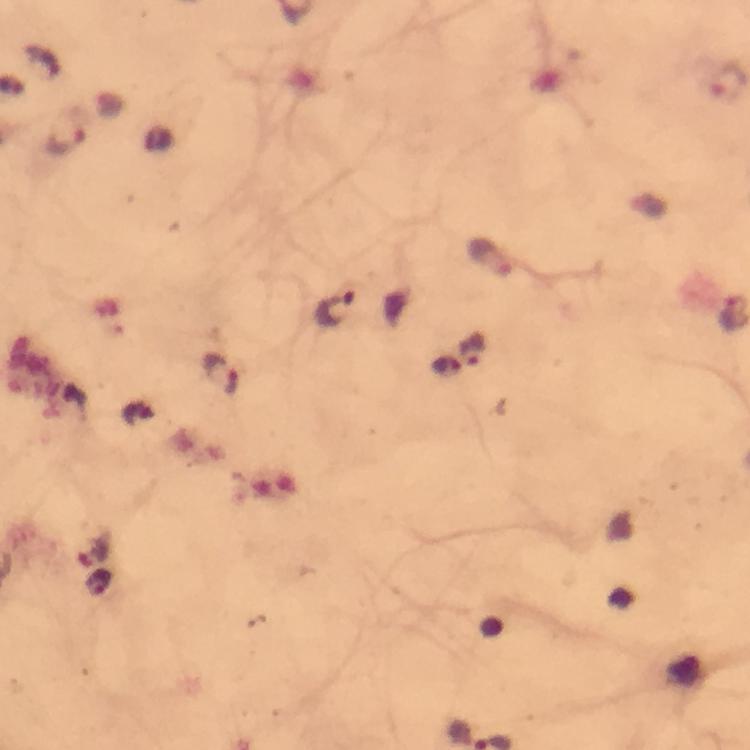
Approximate centers as (x, y) in pixels. Plasmodium parasite locations: (65, 141), (335, 310), (474, 350), (447, 364), (222, 370), (94, 552), (99, 584). Immersion oil applied. From a malaria diagnostic workup. Giemsa-stained preparation. Photographed with a smartphone mounted on the microscope. 100x magnification. Image is 750×750 pixels. Thick blood film. Cropped region of a single field of view.